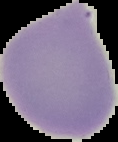

image size = 118×142 pixels
result = negative for Plasmodium parasites
image type = segmented cell region on a black background
preparation = thin blood film